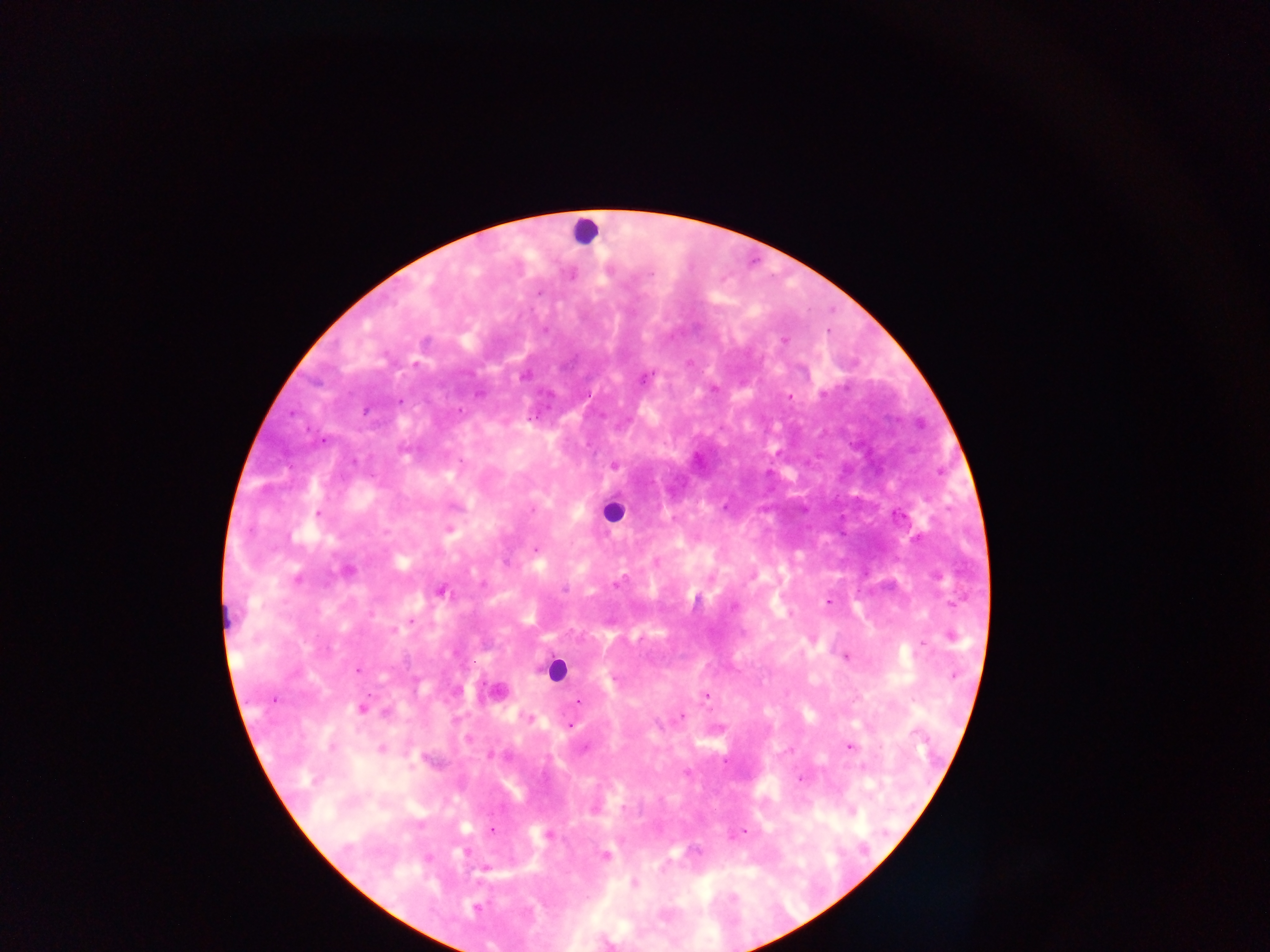

Approximate centers as (x, y) in pixels.
Summary:
  - Malaria parasite locations: (783, 340), (689, 362), (644, 377), (713, 388), (789, 395), (614, 465), (317, 514), (449, 528), (535, 550), (346, 570), (440, 591), (828, 600), (950, 636), (812, 638), (845, 656), (357, 669), (497, 692), (705, 695), (576, 702), (361, 708), (680, 716), (528, 718), (569, 726), (467, 739), (848, 746), (381, 749), (788, 750), (490, 755), (800, 778), (594, 807), (851, 810), (491, 831), (744, 831), (549, 835), (605, 855), (484, 868), (634, 883), (475, 907)
  - Leukocyte locations: (584, 231), (612, 510), (555, 670)
  - Capture: mobile-phone photograph through a microscope
  - Field of view: single
  - Preparation: thick blood smear
  - Image size: 1270×952 pixels
  - Country: Ghana